Report the malaria status of this cell.
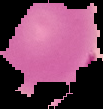
It is parasitized.

{
  "preparation": "thin blood smear",
  "image_type": "segmented cell region with the area outside set to black",
  "image_size": "103×109 pixels"
}